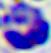

400x magnification. A leukocyte is shown. Photomicrograph.